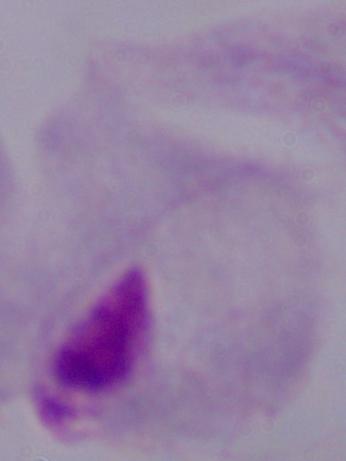

A trichomonad is seen. 1000x magnification. Photomicrograph.